Name the blood parasite species.
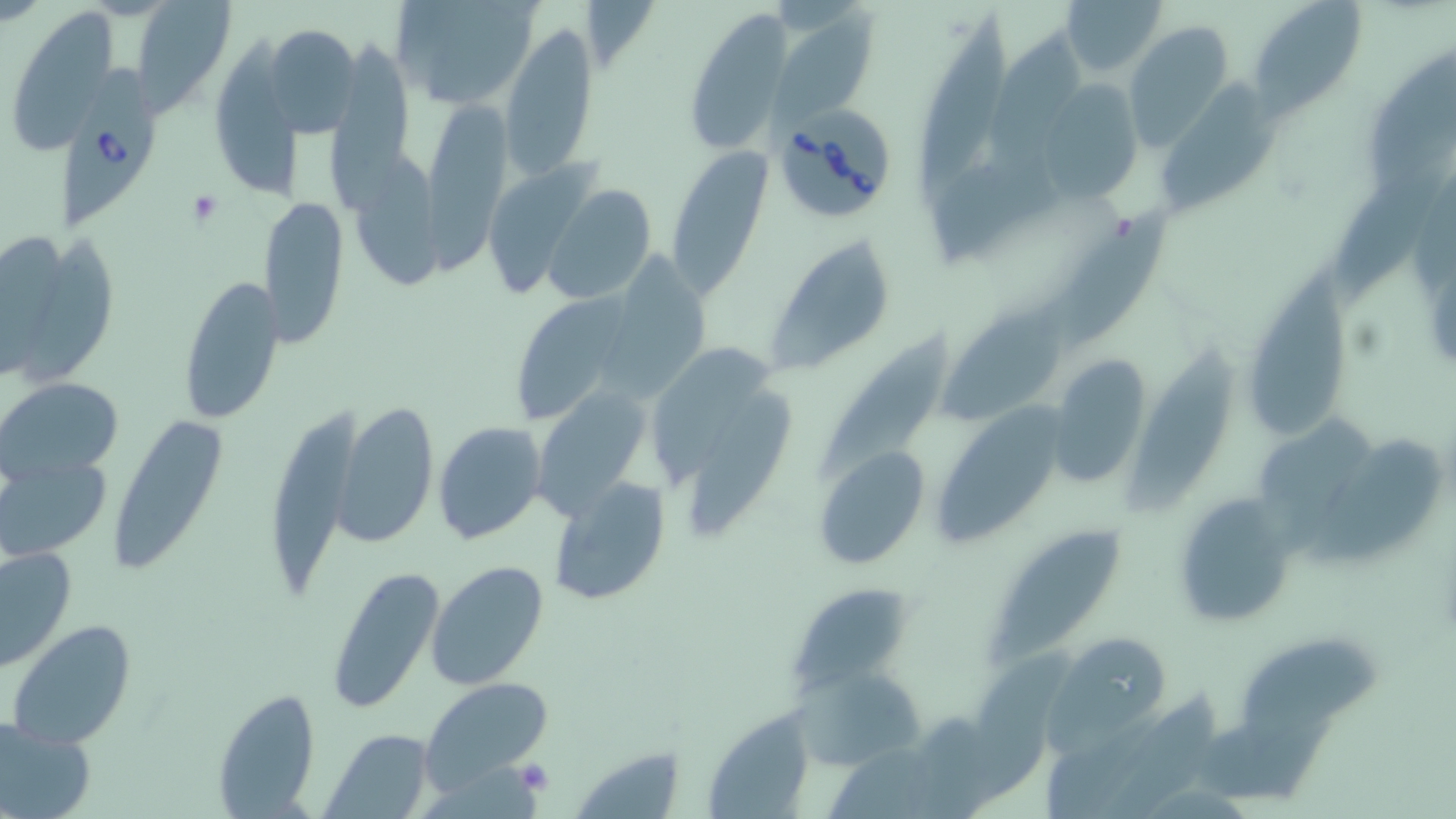

Babesia divergens.

Approximate bounding boxes as [x1, y1, x2, y2] in pixels. Platelet locations: [185, 189, 224, 228], [513, 761, 554, 795]. Uninfected red blood cell locations: [130, 0, 238, 114], [390, 0, 542, 109], [1061, 0, 1167, 79], [1246, 0, 1369, 117], [912, 8, 1012, 194], [13, 9, 121, 157], [688, 9, 791, 150], [760, 15, 877, 125], [502, 21, 598, 181], [1124, 21, 1236, 150], [263, 24, 361, 138], [992, 28, 1087, 176], [327, 32, 416, 218], [212, 36, 306, 198], [1369, 45, 1456, 193], [1158, 78, 1280, 212], [1043, 80, 1146, 205], [425, 102, 511, 280], [663, 145, 772, 298], [353, 153, 448, 290], [1341, 167, 1447, 298], [543, 185, 657, 305], [262, 199, 350, 350], [1051, 202, 1166, 346], [1, 230, 101, 381], [767, 235, 897, 377], [605, 242, 715, 401], [1240, 253, 1354, 440], [177, 274, 286, 426], [517, 292, 638, 425], [942, 308, 1067, 421], [816, 328, 971, 481], [653, 340, 775, 475], [1127, 347, 1237, 509], [1046, 356, 1154, 487], [0, 375, 124, 483], [537, 377, 659, 525], [681, 377, 798, 539], [335, 398, 438, 549], [932, 402, 1074, 547], [268, 403, 365, 602], [103, 415, 230, 578], [433, 420, 547, 543], [1252, 422, 1380, 552], [1311, 444, 1443, 566], [811, 446, 930, 571], [1, 452, 113, 561], [546, 477, 670, 606], [1172, 495, 1295, 626], [995, 528, 1127, 665], [1, 542, 77, 671], [425, 559, 550, 691], [323, 564, 443, 713], [783, 590, 909, 697], [6, 620, 138, 750], [1050, 630, 1172, 737], [1241, 639, 1385, 737], [795, 664, 929, 775], [421, 677, 554, 790], [1094, 684, 1223, 819], [212, 687, 322, 817], [708, 706, 814, 819], [0, 716, 97, 819], [1197, 716, 1341, 803], [322, 729, 436, 814], [573, 745, 689, 818]. Babesia divergens-infected red blood cell locations: [61, 61, 153, 230], [773, 104, 893, 222]. Image is 1456×819 pixels. May-Grünwald-Giemsa stain. Optical microscopy. One field of a larger specimen. Thin blood film. 1000x magnification.